Classify this cell by malaria status.
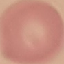

It is uninfected.

Acquired by smartphone through the microscope eyepiece. Giemsa-stained preparation. Thin smear of blood. Cell patch, automatically extracted from a larger field of view and resized to 64 × 64 pixels.